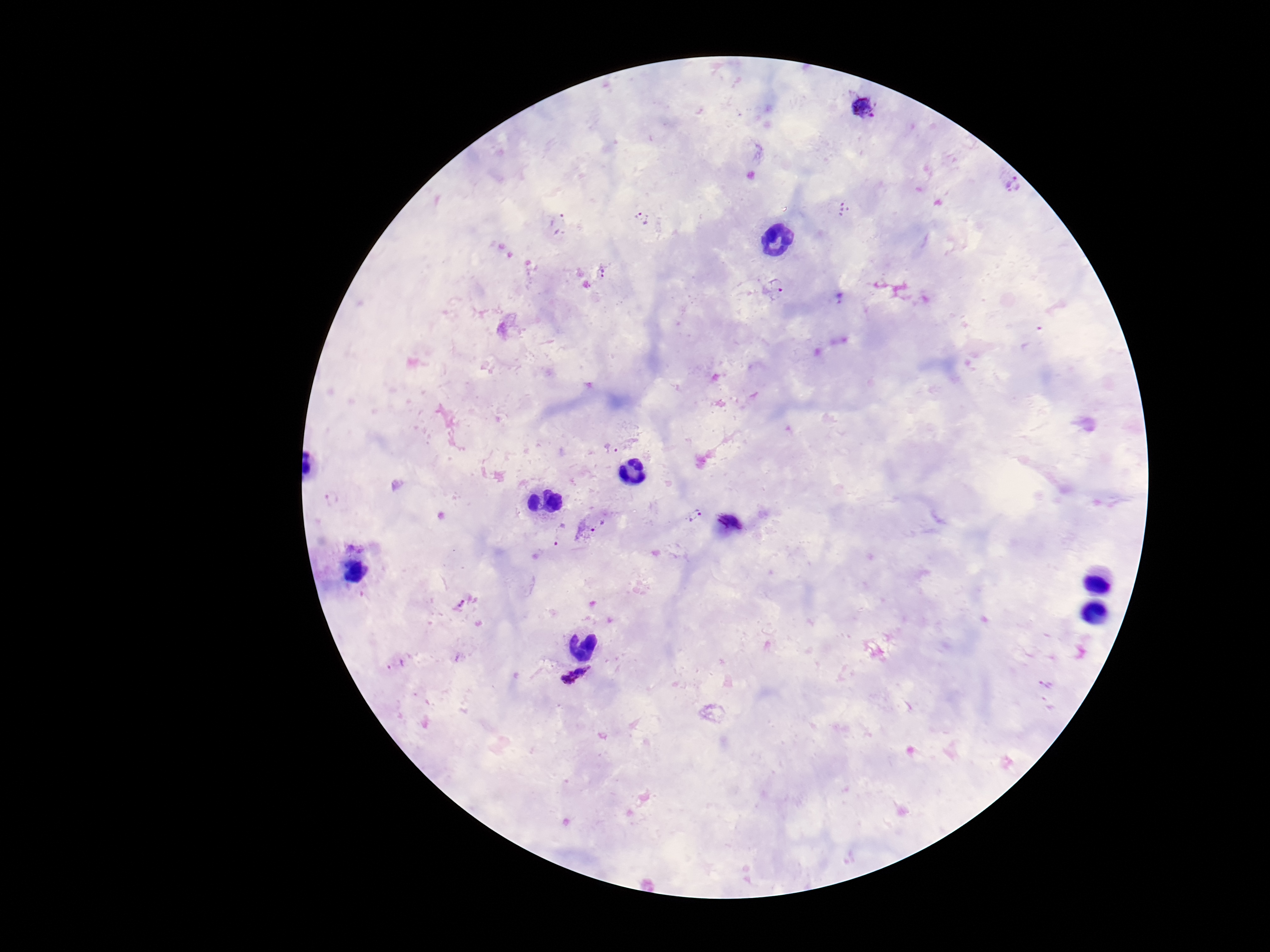

Approximate centers as {x, y} in pixels.
Summary:
  - Plasmodium parasite locations: {863, 107}, {1014, 182}, {844, 210}, {643, 218}, {559, 225}, {602, 273}, {776, 289}, {840, 298}, {331, 498}, {694, 515}, {599, 528}, {558, 535}, {461, 605}, {396, 665}, {575, 676}
  - Field of view: single
  - Capture: smartphone camera through the microscope eyepiece
  - Magnification: 100x
  - Patient malaria status: positive
  - Preparation: thick blood smear
  - Stain: Giemsa
  - Image size: 1270×952 pixels